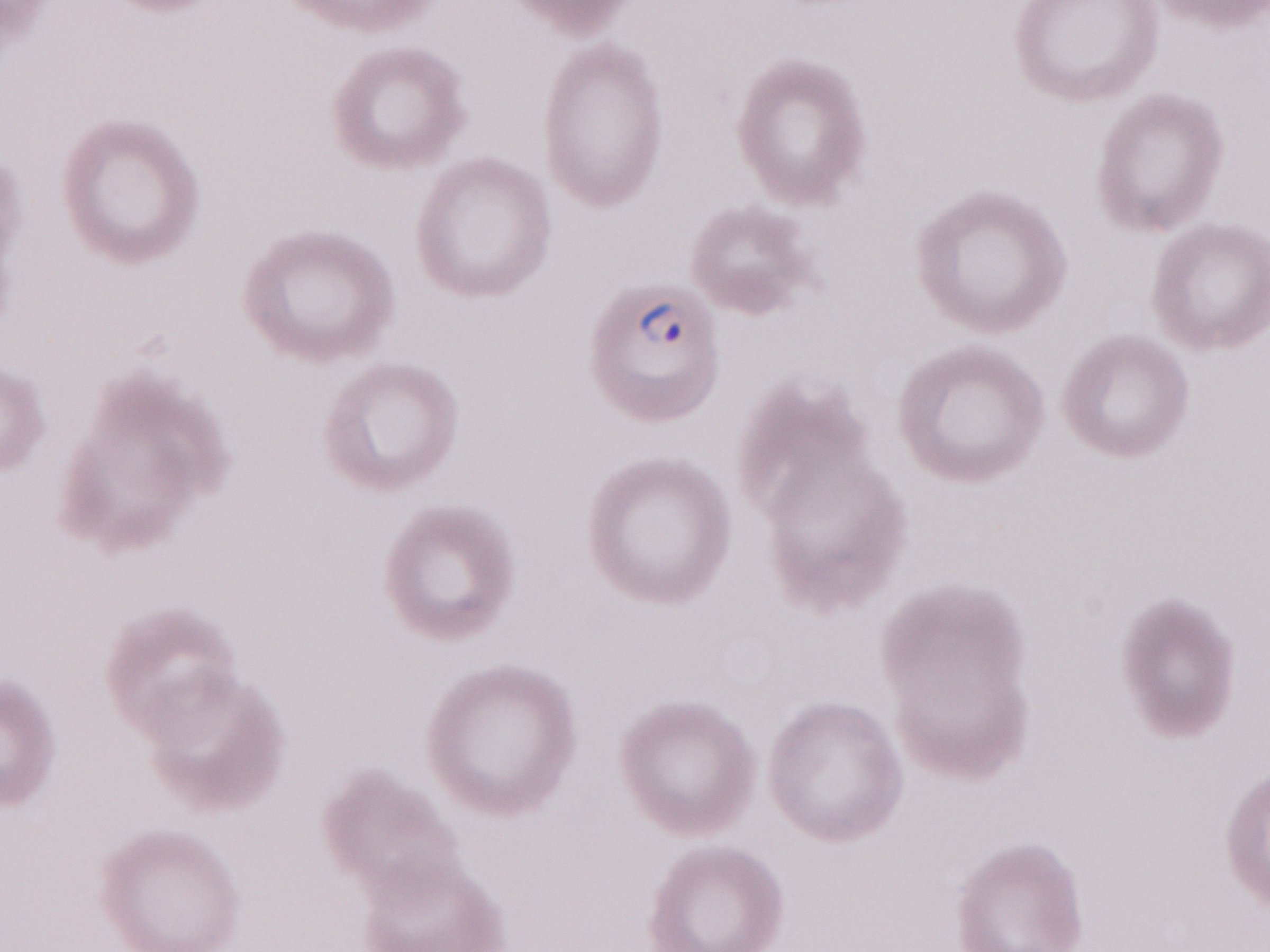
Olympus BX43 microscope, Olympus DP73 camera. Patient-level malaria diagnosis: positive. 1,000x magnification. One field of this slide. May-Grünwald-Giemsa (MGG) stain. Image is 1270×952 pixels. Thin blood smear.